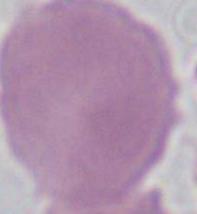 Micrograph. 1000x magnification. A red blood cell is shown.